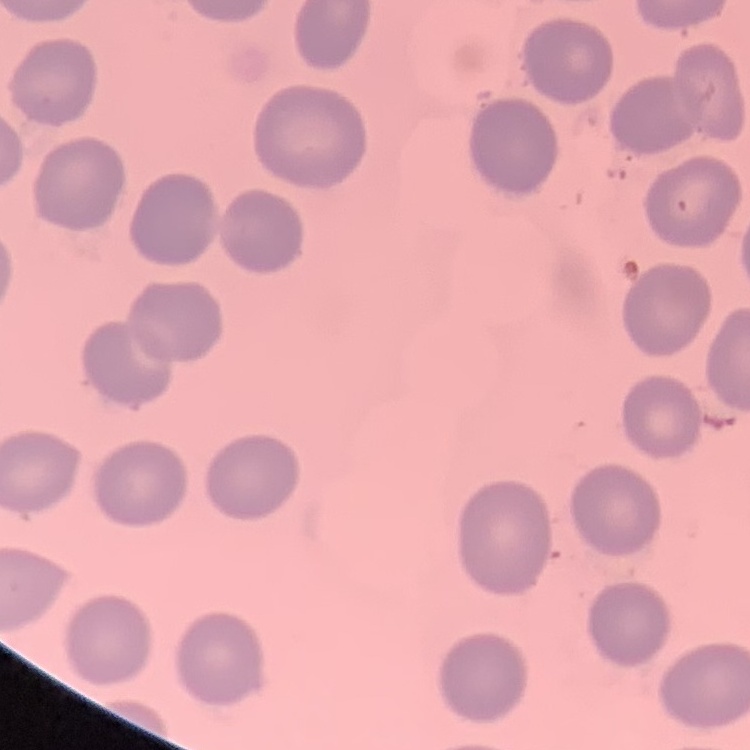
Summary:
  - Erythrocyte morphology: no rouleaux formation
  - Image type: square crop of a larger photomicrograph
  - Stain: Field's or Giemsa
  - Preparation: thin peripheral smear